Assess this cell for malaria.
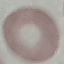
Uninfected.

Summary:
  - Image type: automatically extracted cell patch, resized to 64 × 64 pixels
  - Stain: Giemsa
  - Preparation: thin blood film
  - Capture: smartphone camera at the microscope eyepiece